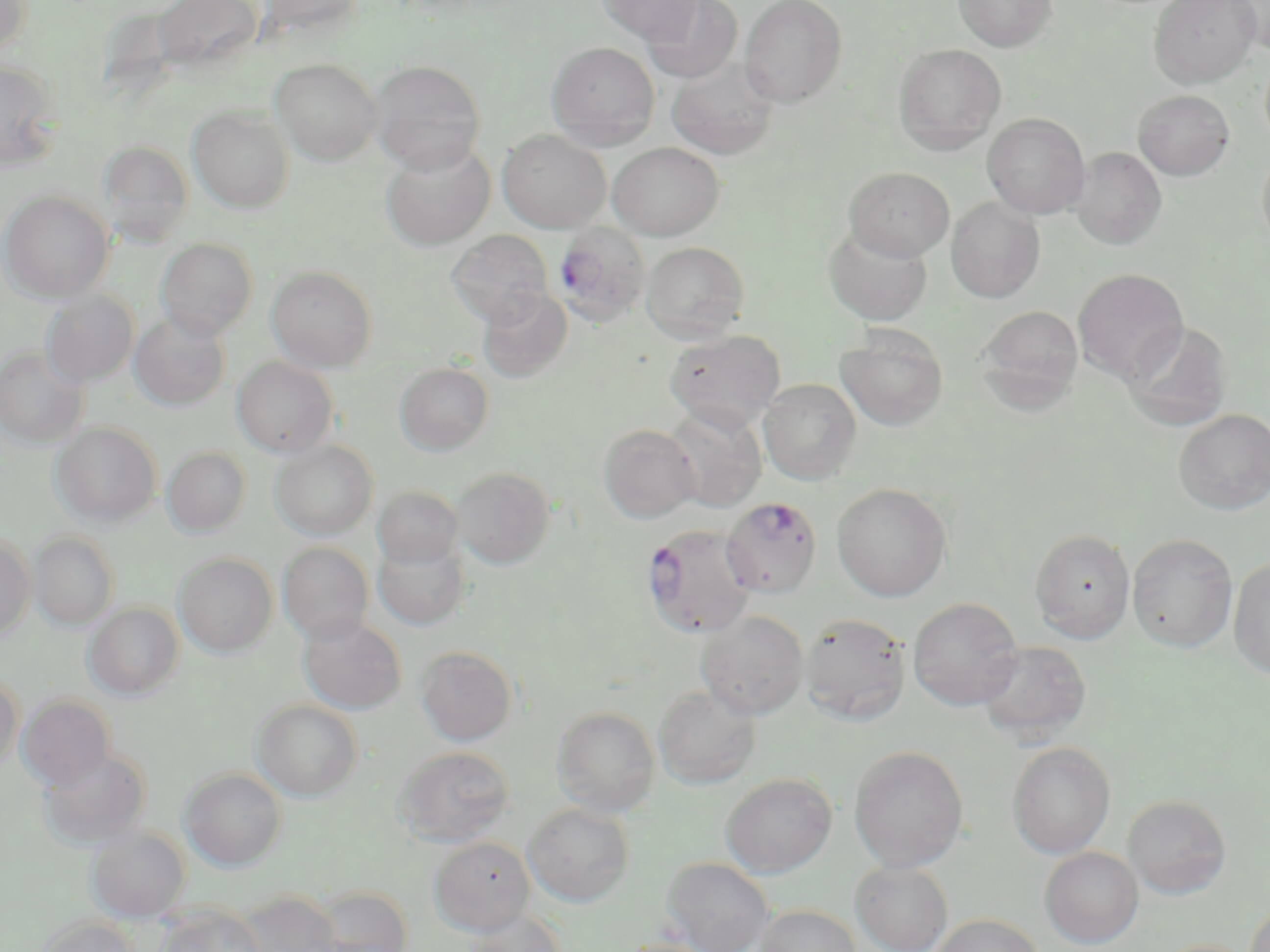
Summary:
  - Coordinate format: approximate bounding boxes as [x1, y1, x2, y2] in pixels
  - Uninfected red blood cell locations: [152, 0, 263, 78], [257, 0, 366, 39], [597, 0, 703, 44], [641, 0, 743, 84], [739, 0, 848, 108], [952, 0, 1058, 52], [1149, 0, 1262, 88], [0, 1, 33, 57], [1227, 1, 1270, 54], [546, 41, 660, 149], [893, 43, 1007, 153], [667, 58, 779, 160], [0, 59, 64, 172], [270, 59, 382, 165], [368, 59, 486, 174], [1133, 89, 1234, 180], [188, 106, 295, 213], [982, 113, 1090, 219], [497, 129, 611, 233], [99, 140, 193, 247], [380, 141, 495, 251], [608, 142, 724, 240], [1257, 144, 1270, 257], [1071, 146, 1166, 249], [844, 167, 954, 261], [1, 190, 113, 303], [946, 197, 1045, 303], [824, 224, 933, 325], [446, 230, 553, 326], [156, 238, 258, 341], [641, 241, 750, 342], [266, 265, 378, 372], [1073, 268, 1189, 384], [478, 287, 572, 383], [41, 291, 139, 387], [976, 305, 1084, 410], [129, 313, 230, 411], [1123, 321, 1233, 431], [664, 329, 785, 431], [836, 329, 948, 431], [0, 346, 89, 449], [231, 357, 338, 458], [394, 363, 494, 456], [758, 379, 862, 484], [664, 405, 767, 512], [1174, 409, 1270, 515], [51, 422, 161, 527], [598, 423, 702, 523], [270, 440, 378, 540], [162, 447, 251, 537], [452, 467, 555, 569], [832, 483, 952, 601], [373, 486, 464, 570], [1031, 528, 1135, 642], [29, 531, 120, 630], [0, 533, 35, 641], [1128, 533, 1237, 652], [372, 536, 471, 631], [277, 542, 375, 644], [173, 553, 278, 658], [1229, 556, 1270, 680], [908, 597, 1023, 710], [84, 602, 185, 700], [696, 610, 808, 719], [800, 612, 911, 725], [298, 615, 406, 715], [976, 640, 1091, 744], [415, 645, 518, 746], [0, 671, 23, 772], [654, 685, 761, 788], [17, 694, 116, 790], [252, 699, 363, 801], [552, 706, 660, 816], [1007, 741, 1115, 859], [849, 745, 969, 872], [394, 746, 515, 847], [38, 747, 152, 848], [180, 767, 287, 871], [720, 773, 836, 877], [1123, 794, 1232, 899], [523, 803, 634, 907], [85, 826, 190, 922], [429, 836, 534, 936], [1040, 847, 1143, 948], [660, 856, 774, 952], [850, 860, 953, 952], [308, 885, 413, 952], [236, 890, 341, 952], [1244, 900, 1270, 952], [156, 904, 265, 952], [754, 904, 862, 952], [463, 909, 567, 951], [929, 913, 1044, 952], [37, 916, 140, 952], [614, 937, 721, 952], [1153, 938, 1259, 952]
  - Plasmodium falciparum-infected red blood cell locations: [552, 222, 651, 328], [720, 496, 823, 598], [641, 523, 757, 638]
  - Slide-level diagnosis: Plasmodium falciparum
  - Magnification: 1000x
  - Field of view: single
  - Stain: May-Grünwald-Giemsa
  - Modality: light microscopy
  - Image size: 1270×952 pixels
  - Preparation: thin blood film